Locate every blood parasite and identify its species.
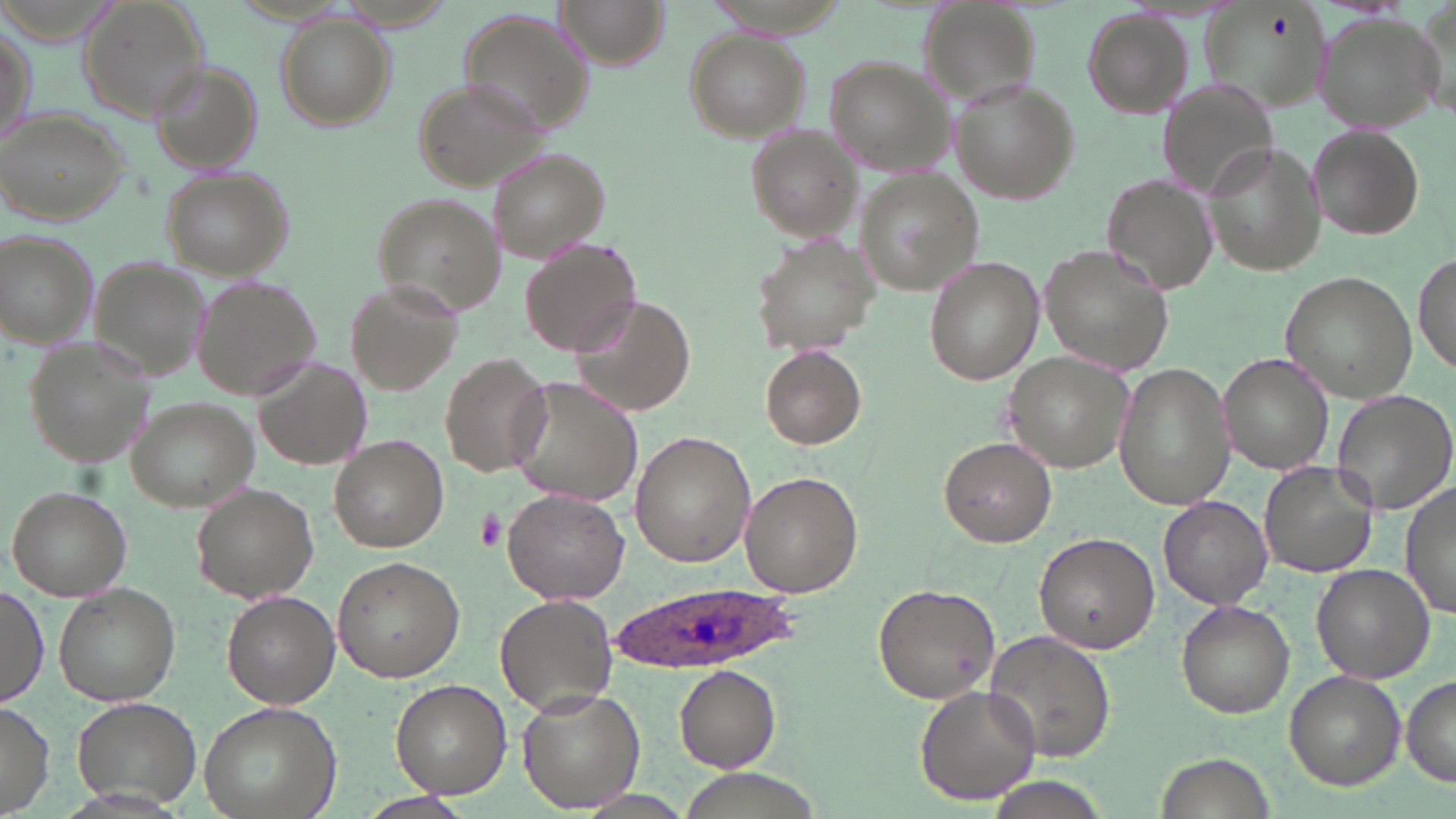
Approximate bounding boxes as named x1/y1/x2/y2 corners in pixels.
Plasmodium ovale-infected red blood cells: (x1=610, y1=581, x2=796, y2=673).
No Plasmodium falciparum, Plasmodium malariae, Plasmodium vivax, Babesia divergens, or Trypanosoma brucei observed.

Uninfected red blood cell locations: (x1=74, y1=0, x2=212, y2=120), (x1=557, y1=0, x2=669, y2=66), (x1=1200, y1=3, x2=1331, y2=117), (x1=1084, y1=11, x2=1192, y2=118), (x1=460, y1=12, x2=599, y2=139), (x1=1311, y1=14, x2=1443, y2=130), (x1=274, y1=18, x2=394, y2=131), (x1=1, y1=19, x2=36, y2=152), (x1=684, y1=31, x2=809, y2=142), (x1=821, y1=56, x2=955, y2=173), (x1=149, y1=60, x2=264, y2=170), (x1=1158, y1=74, x2=1278, y2=201), (x1=413, y1=78, x2=554, y2=193), (x1=948, y1=79, x2=1078, y2=204), (x1=0, y1=108, x2=130, y2=224), (x1=740, y1=125, x2=863, y2=241), (x1=1309, y1=127, x2=1426, y2=238), (x1=1203, y1=143, x2=1321, y2=276), (x1=486, y1=148, x2=609, y2=264), (x1=159, y1=167, x2=294, y2=280), (x1=854, y1=172, x2=988, y2=296), (x1=1101, y1=175, x2=1221, y2=298), (x1=371, y1=194, x2=506, y2=318), (x1=2, y1=229, x2=100, y2=350), (x1=749, y1=232, x2=878, y2=356), (x1=518, y1=237, x2=643, y2=358), (x1=1039, y1=244, x2=1171, y2=373), (x1=1415, y1=248, x2=1453, y2=381), (x1=925, y1=257, x2=1044, y2=385), (x1=90, y1=259, x2=213, y2=384), (x1=1280, y1=271, x2=1420, y2=402), (x1=193, y1=276, x2=326, y2=401), (x1=348, y1=290, x2=461, y2=398), (x1=569, y1=294, x2=698, y2=418), (x1=21, y1=334, x2=152, y2=472), (x1=761, y1=346, x2=866, y2=448), (x1=1003, y1=352, x2=1137, y2=472), (x1=255, y1=353, x2=371, y2=471), (x1=440, y1=353, x2=553, y2=479), (x1=1220, y1=354, x2=1334, y2=474), (x1=1113, y1=360, x2=1234, y2=510), (x1=506, y1=375, x2=645, y2=510), (x1=1331, y1=388, x2=1455, y2=515), (x1=126, y1=396, x2=260, y2=510), (x1=631, y1=432, x2=755, y2=566), (x1=330, y1=435, x2=449, y2=552), (x1=938, y1=435, x2=1056, y2=547), (x1=1258, y1=460, x2=1378, y2=580), (x1=739, y1=471, x2=864, y2=597), (x1=1399, y1=482, x2=1456, y2=619), (x1=189, y1=483, x2=320, y2=603), (x1=8, y1=486, x2=131, y2=601), (x1=502, y1=487, x2=629, y2=605), (x1=1157, y1=496, x2=1274, y2=608), (x1=1033, y1=533, x2=1160, y2=654), (x1=332, y1=555, x2=463, y2=682), (x1=1310, y1=562, x2=1436, y2=683), (x1=53, y1=582, x2=181, y2=707), (x1=873, y1=583, x2=998, y2=705), (x1=0, y1=584, x2=49, y2=707), (x1=221, y1=591, x2=337, y2=708), (x1=496, y1=593, x2=619, y2=718), (x1=1175, y1=599, x2=1293, y2=717), (x1=983, y1=629, x2=1117, y2=764), (x1=676, y1=666, x2=781, y2=772), (x1=1285, y1=670, x2=1404, y2=789), (x1=1403, y1=675, x2=1456, y2=787), (x1=391, y1=679, x2=511, y2=797), (x1=914, y1=684, x2=1042, y2=807), (x1=516, y1=687, x2=643, y2=812), (x1=71, y1=695, x2=206, y2=809), (x1=198, y1=699, x2=339, y2=819), (x1=0, y1=703, x2=55, y2=815), (x1=1154, y1=751, x2=1276, y2=819), (x1=983, y1=779, x2=1107, y2=819). Platelet locations: (x1=475, y1=508, x2=507, y2=551). Slide-level diagnosis: Plasmodium ovale. Image is 1456×819 pixels. Thin blood smear. Captured at 1000x magnification. One field of a larger specimen. May-Grünwald-Giemsa stain. Optical microscopy.